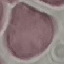
Summary:
  - Result: no malaria parasites detected
  - Image type: automatically extracted cell patch, resized to 64 × 64 pixels
  - Stain: Giemsa
  - Capture: smartphone camera at the microscope eyepiece
  - Preparation: thin blood smear